Report the malaria status of this cell.
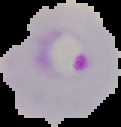

Parasitized.

From a thin blood film. Segmented cell region on a black background. Image is 121×127 pixels.